Describe the morphology of the erythrocytes.
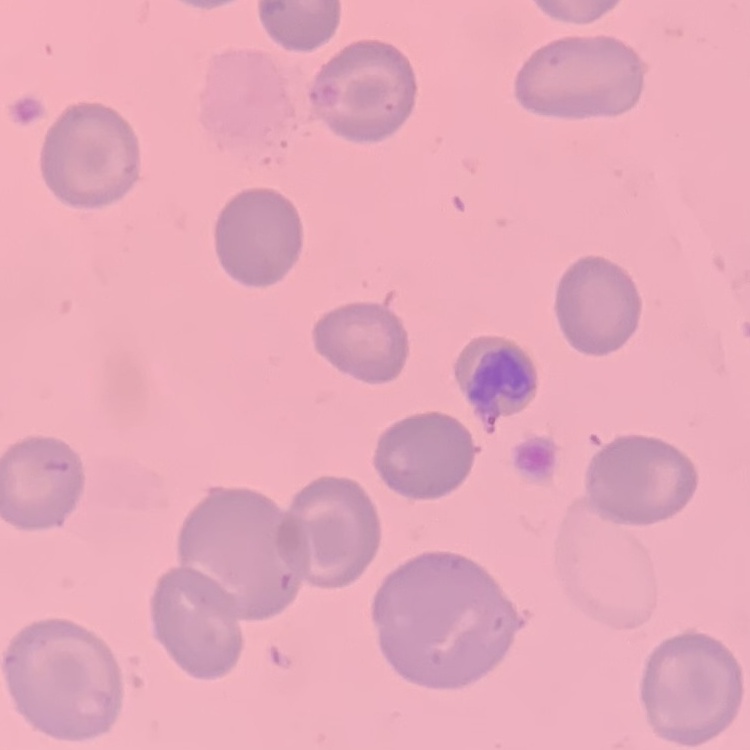
They show no rouleaux formation.

Thin peripheral smear. Field's or Giemsa stain. One tile cut from a larger photomicrograph.